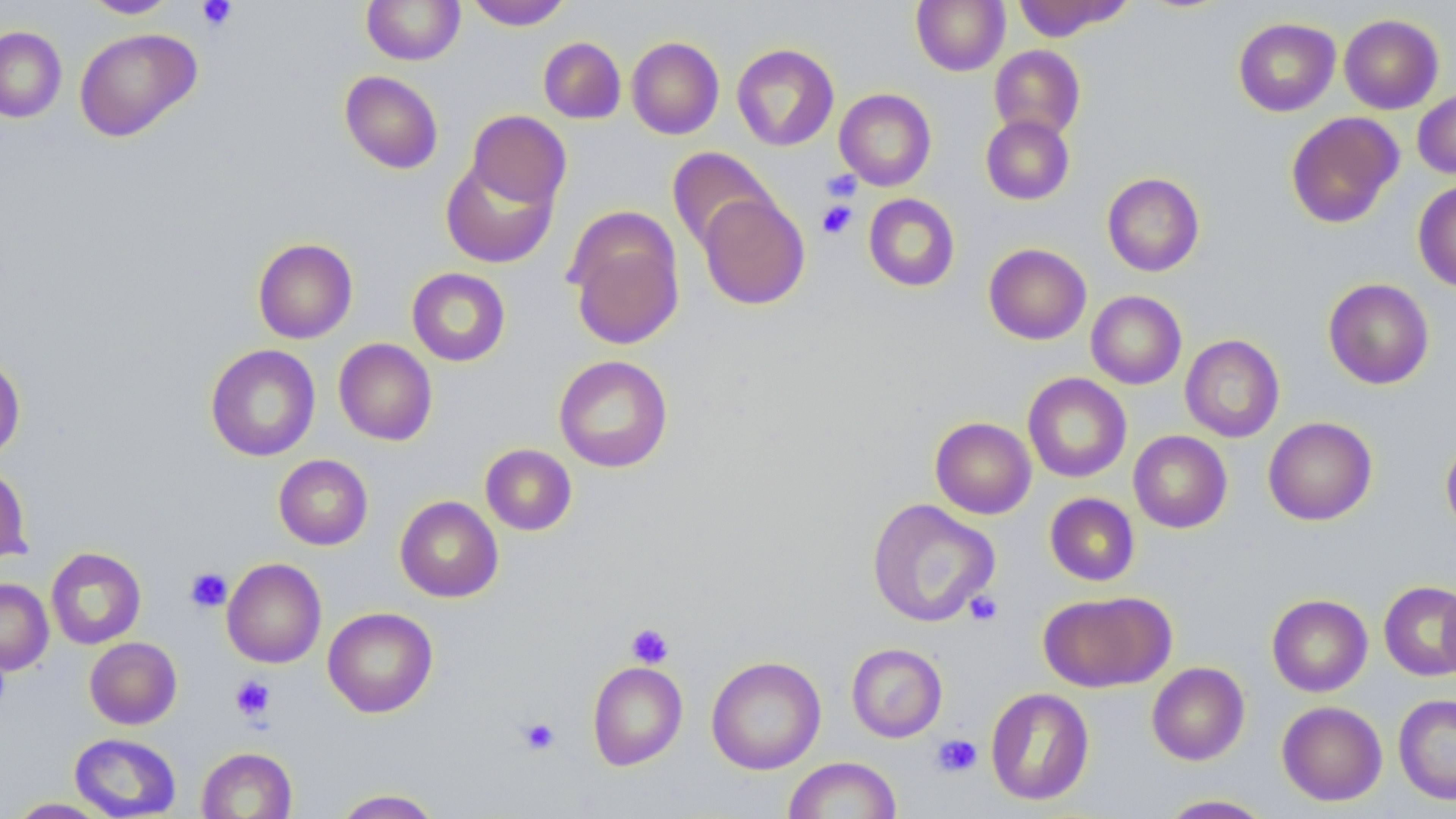

slide-level diagnosis = negative for blood parasites
stain = May-Grünwald-Giemsa
modality = optical microscopy
field of view = single
platelet locations = approximate bounding boxes as (x1, y1, x2, y2) in pixels: (196, 0, 237, 32), (821, 168, 862, 202), (816, 200, 857, 239), (185, 568, 232, 613), (964, 590, 1003, 626), (626, 622, 674, 669), (230, 675, 275, 722), (517, 716, 560, 755), (930, 733, 982, 778)
magnification = 1000x
image size = 1456×819 pixels
preparation = thin blood smear
uninfected red blood cell locations = approximate bounding boxes as (x1, y1, x2, y2) in pixels: (80, 0, 180, 18), (361, 0, 465, 65), (467, 0, 571, 30), (911, 0, 1009, 76), (1013, 0, 1129, 41), (1339, 14, 1444, 114), (1233, 17, 1340, 117), (0, 26, 66, 123), (74, 27, 202, 142), (626, 36, 724, 139), (538, 37, 626, 124), (731, 43, 839, 151), (989, 44, 1085, 141), (339, 71, 443, 174), (834, 88, 936, 191), (1413, 89, 1456, 179), (467, 110, 570, 209), (1285, 111, 1403, 229), (981, 114, 1074, 205), (667, 147, 778, 253), (441, 156, 558, 269), (1102, 172, 1204, 276), (1413, 180, 1456, 291), (863, 193, 960, 291), (697, 194, 810, 310), (566, 214, 685, 352), (252, 238, 358, 343), (983, 243, 1091, 345), (406, 267, 511, 366), (1323, 278, 1434, 389), (1086, 291, 1187, 389), (1180, 334, 1285, 442), (333, 338, 437, 446), (205, 344, 320, 461), (0, 353, 25, 461), (554, 355, 673, 472), (1023, 373, 1132, 482), (930, 417, 1036, 519), (1263, 417, 1377, 525), (1129, 430, 1232, 533), (1441, 437, 1456, 535), (480, 444, 577, 535), (274, 454, 373, 550), (0, 463, 32, 565), (1045, 493, 1140, 586), (395, 496, 503, 602), (867, 499, 1000, 627), (46, 547, 146, 649), (222, 558, 327, 668), (0, 578, 53, 675), (1379, 581, 1456, 681), (1439, 582, 1456, 682), (1038, 591, 1174, 692), (1267, 594, 1373, 697), (322, 607, 438, 717), (84, 637, 182, 729), (846, 643, 948, 742), (706, 656, 826, 775), (587, 661, 687, 770), (1147, 662, 1250, 765), (985, 687, 1095, 806), (1393, 693, 1456, 805), (1277, 701, 1387, 806), (69, 733, 181, 818), (196, 746, 297, 819), (783, 756, 902, 818), (332, 789, 443, 818), (1157, 794, 1275, 818), (6, 797, 114, 818)